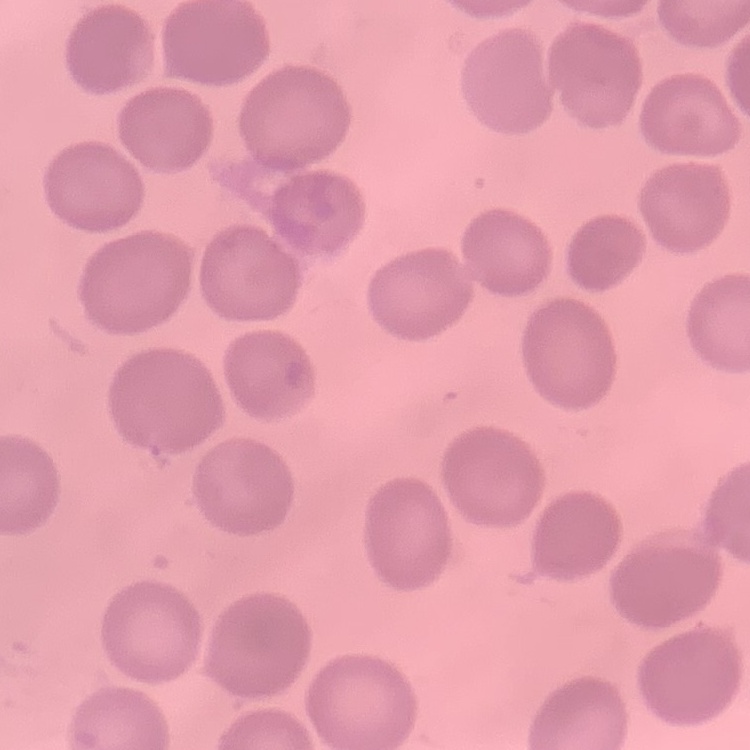

The erythrocytes show no rouleaux formation. Field's or Giemsa stain. Thin peripheral smear. One tile cut from a larger photomicrograph.